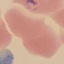

malaria status = parasitized
stain = Giemsa
preparation = thin blood film
capture = smartphone camera at the microscope eyepiece
image type = automatically extracted cell patch, resized to 64 × 64 pixels